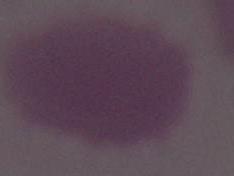 A red blood cell is seen. 1000x magnification. Micrograph.